Comment on the morphology of the erythrocytes.
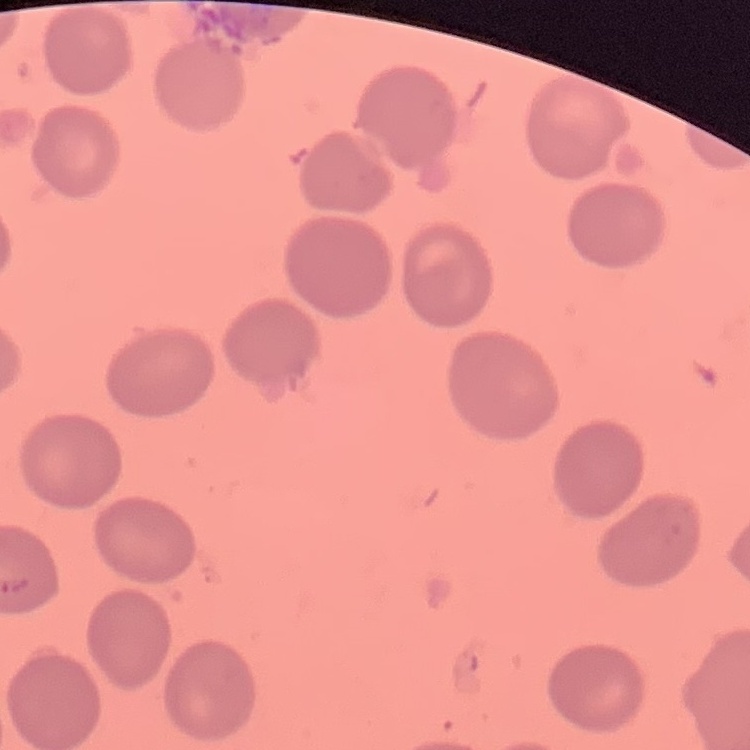

No rouleaux formation.

Summary:
  - Image type: one tile cut from a larger photomicrograph
  - Stain: Field's or Giemsa
  - Preparation: thin blood film